Assess the morphology of the red blood cells.
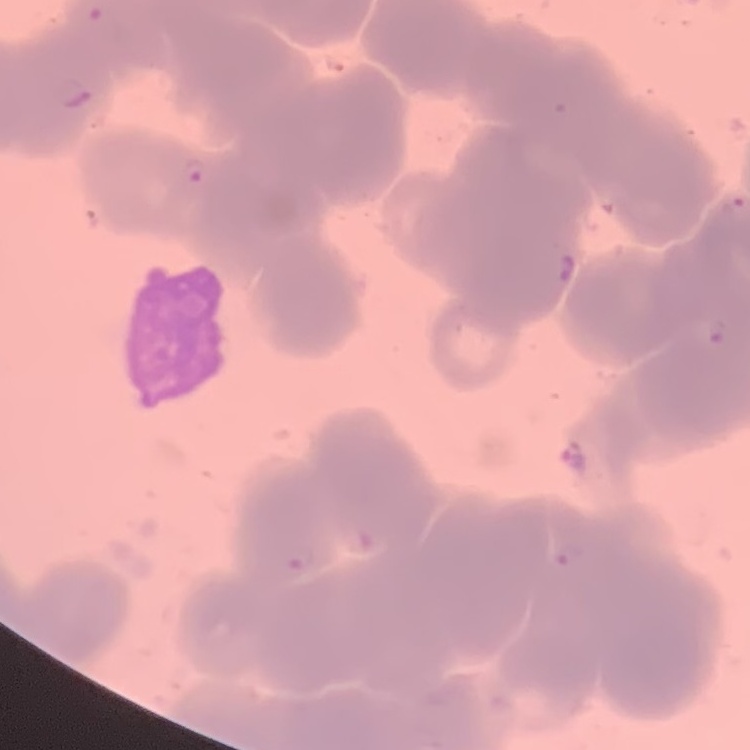

Rouleaux formation.

{
  "preparation": "thin blood smear",
  "image_type": "one tile cut from a larger photomicrograph",
  "stain": "Field's or Giemsa"
}